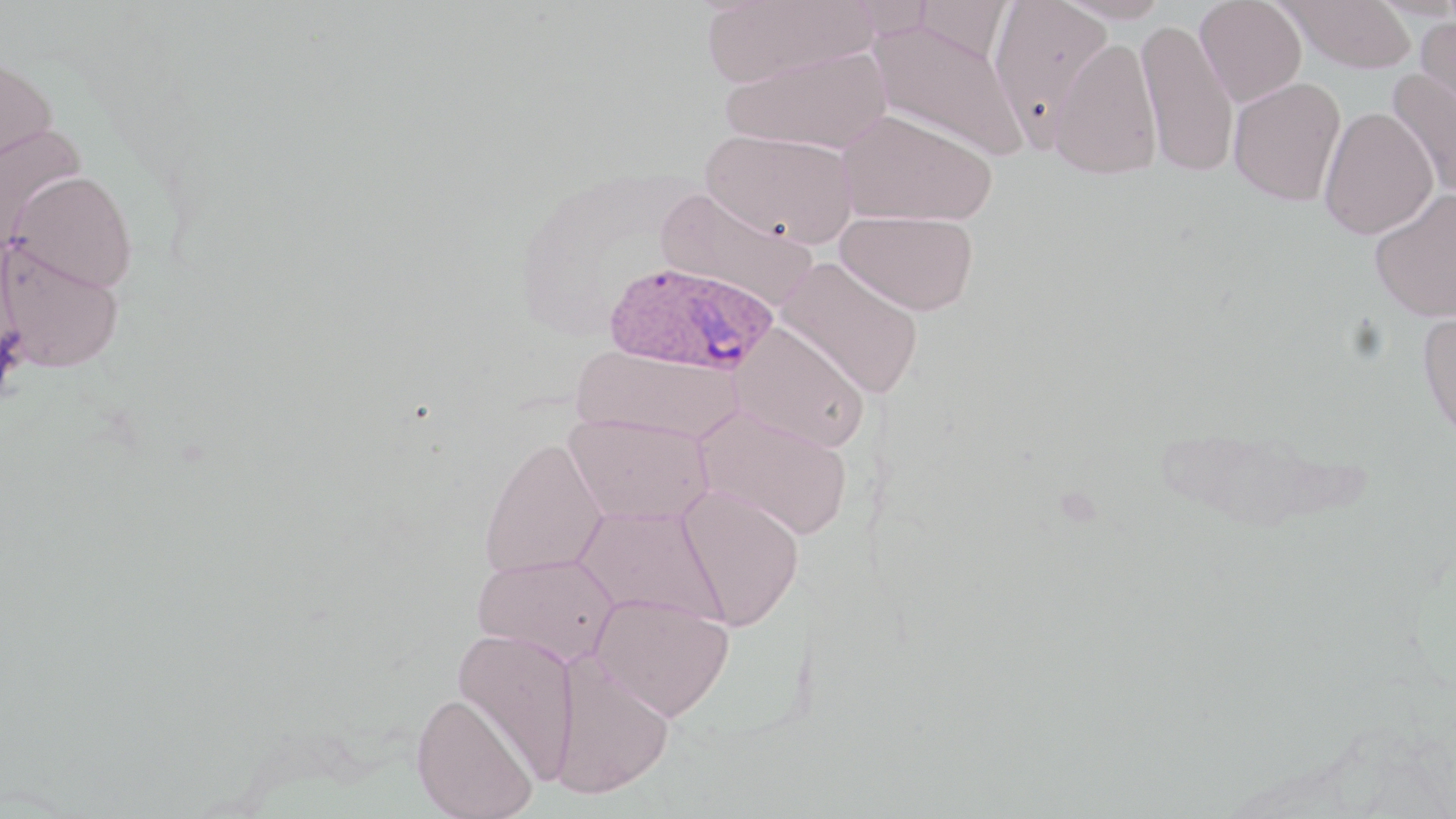
Approximate bounding boxes as [x1, y1, x2, y2] in pixels. Uninfected red blood cell locations: [700, 0, 875, 88], [912, 0, 1012, 63], [988, 0, 1114, 139], [1055, 0, 1171, 23], [1195, 0, 1307, 106], [1281, 0, 1416, 73], [1137, 17, 1239, 179], [1413, 17, 1456, 120], [868, 19, 1027, 161], [1049, 36, 1163, 180], [720, 47, 891, 154], [0, 55, 57, 170], [1387, 69, 1456, 200], [1227, 76, 1346, 206], [1319, 106, 1438, 239], [837, 109, 996, 227], [0, 123, 87, 247], [702, 130, 857, 247], [10, 171, 138, 293], [1368, 187, 1456, 322], [656, 188, 817, 310], [835, 210, 979, 315], [0, 238, 125, 373], [775, 256, 924, 399], [1416, 308, 1456, 448], [731, 322, 870, 452], [572, 345, 743, 445], [694, 404, 854, 541], [564, 413, 714, 525], [479, 436, 608, 579], [674, 486, 806, 629], [573, 506, 724, 624], [472, 553, 619, 666], [591, 592, 733, 721], [452, 628, 580, 782], [548, 651, 674, 799], [411, 692, 538, 819]. Plasmodium ovale-infected red blood cell locations: [605, 260, 777, 377]. Slide-level diagnosis: Plasmodium ovale. One field of a larger specimen. Thin blood smear. Light microscopy. May-Grünwald-Giemsa-stained preparation. 1000x magnification. Image is 1456×819 pixels.